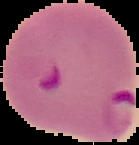

preparation = thin blood film
result = Plasmodium parasites detected
image type = cell region segmented out of the field of view; surrounding area masked to black
image size = 139×145 pixels